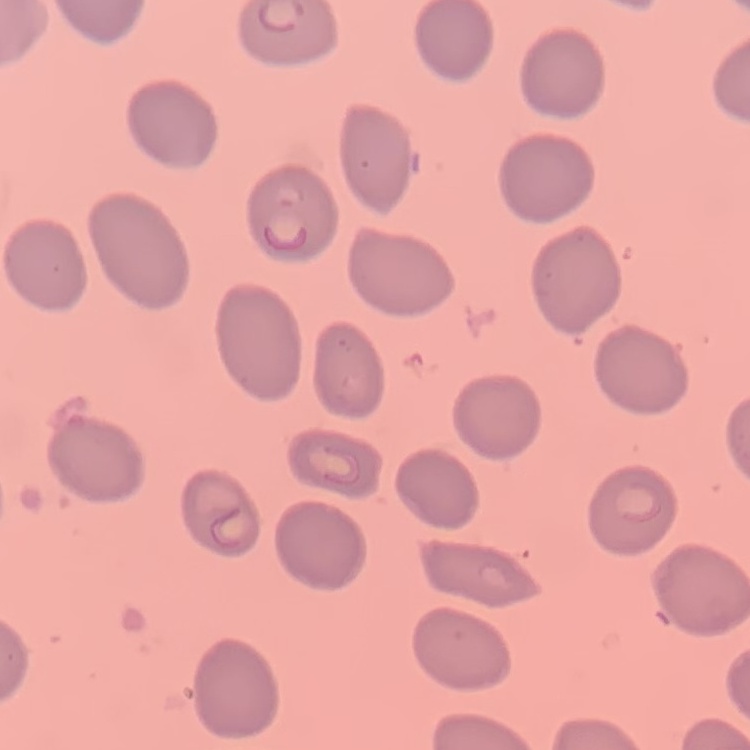

red_blood_cell_morphology: no rouleaux formation
stain: Field's or Giemsa
preparation: thin blood smear
image_type: square crop of a larger photomicrograph